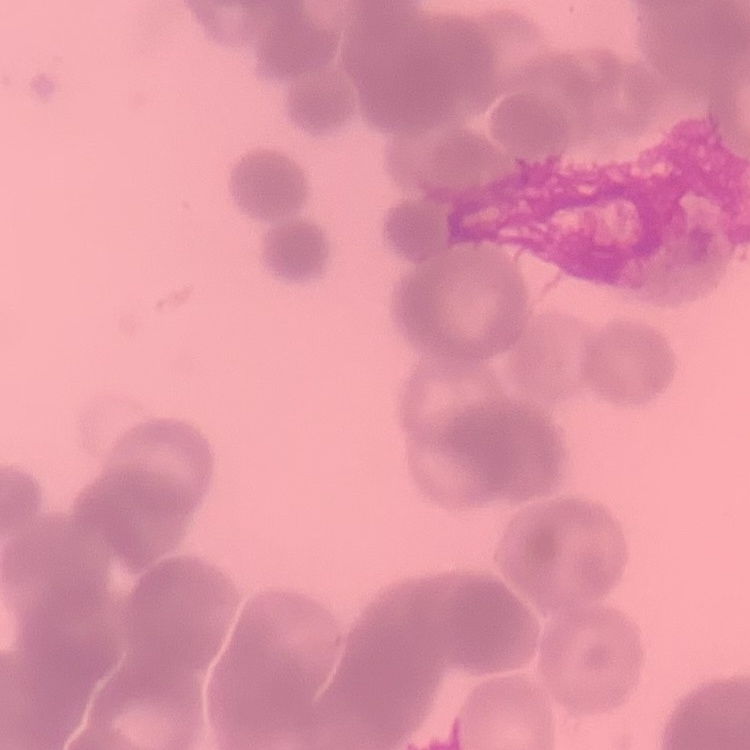
Summary:
  - Red blood cell morphology: rouleaux formation
  - Stain: Field's or Giemsa
  - Image type: one tile cut from a larger photomicrograph
  - Preparation: thin blood film